Assess this cell for malaria.
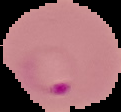
It is parasitized.

The area outside the segmented cell region is set to black. From a thin blood film. Image is 121×112 pixels.